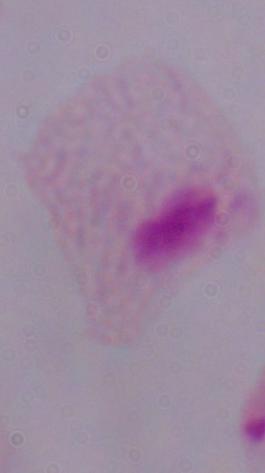
identification = trichomonad
modality = micrograph
magnification = 1000x